Name the parasite shown.
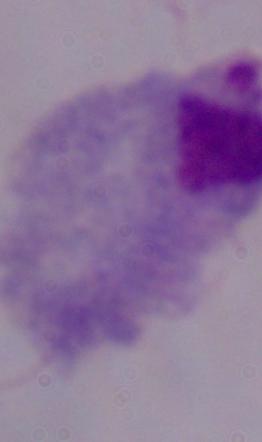
This is a trichomonad.

{
  "modality": "photomicrograph",
  "magnification": "1000x"
}